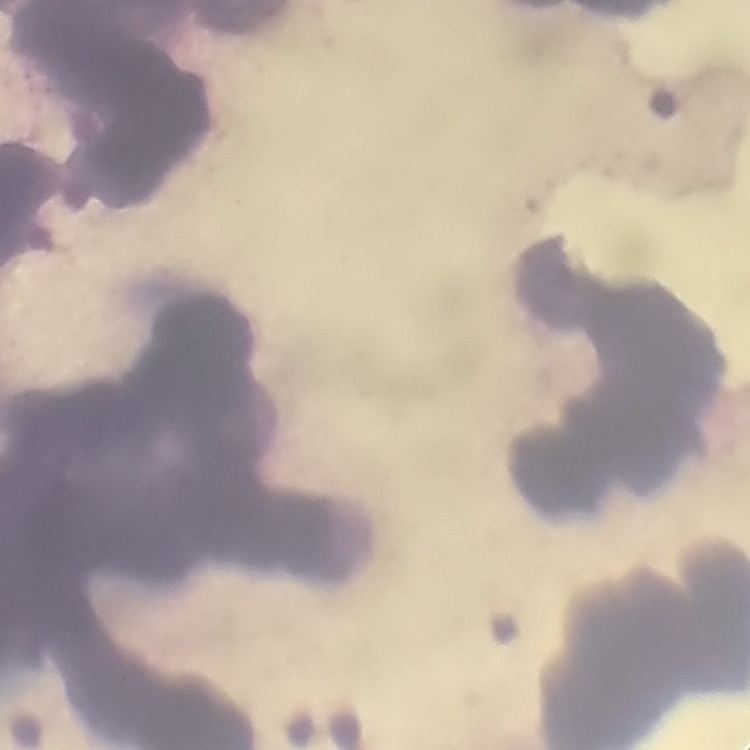

red blood cell morphology = rouleaux formation
image type = one tile cut from a larger photomicrograph
stain = Field's or Giemsa
preparation = thin peripheral smear